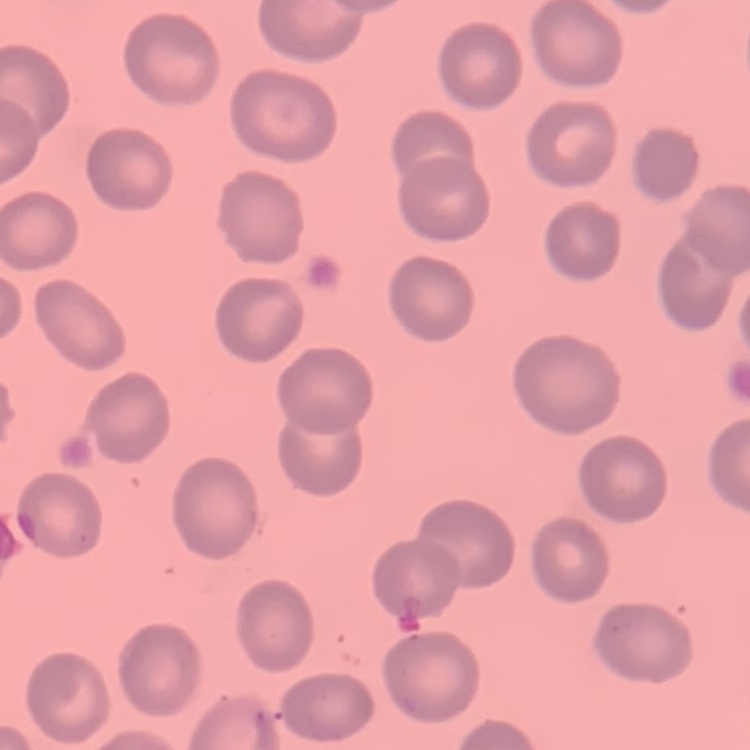
red blood cell morphology = no rouleaux formation
image type = one tile cut from a larger photomicrograph
preparation = thin blood smear
stain = Field's or Giemsa